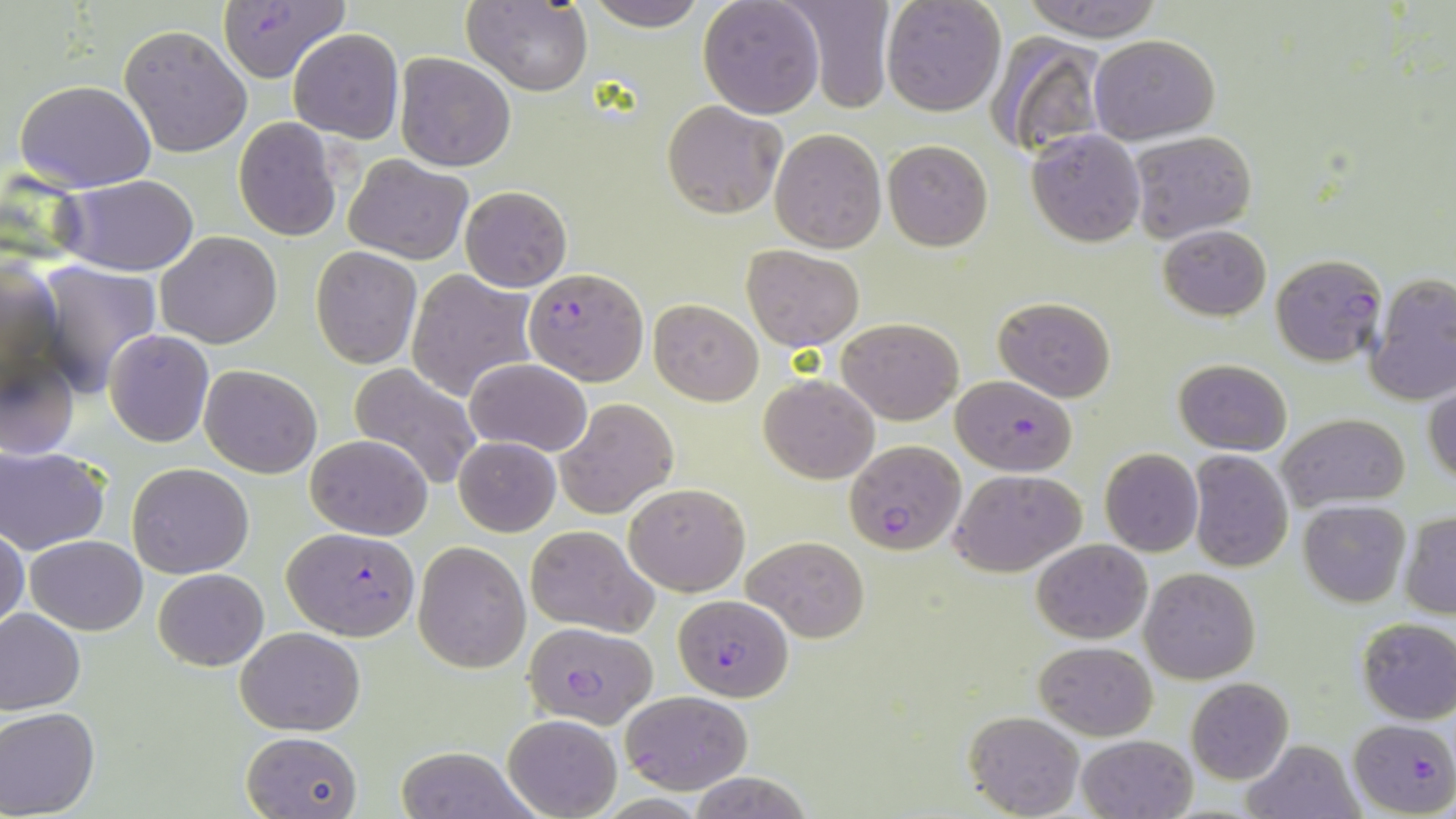
Approximate bounding boxes as (x1,y1)-(x2,y2) corner pairs in pixels. Uninfected red blood cell locations: (588,0)-(709,30), (696,0)-(825,119), (782,0)-(895,110), (880,0)-(1005,117), (1020,0)-(1164,41), (463,1)-(593,95), (119,24)-(253,158), (288,28)-(403,143), (987,32)-(1109,160), (1088,34)-(1219,143), (394,52)-(518,172), (252,54)-(377,204), (14,79)-(157,191), (662,101)-(785,218), (232,117)-(342,243), (1027,127)-(1145,247), (771,128)-(887,252), (1129,128)-(1256,243), (883,140)-(994,251), (343,155)-(472,263), (58,175)-(199,274), (460,185)-(571,292), (1158,223)-(1271,321), (157,231)-(283,348), (743,245)-(865,350), (311,246)-(423,368), (1271,253)-(1388,367), (1,257)-(63,402), (37,261)-(164,395), (409,268)-(534,401), (1365,274)-(1456,405), (994,296)-(1117,402), (649,299)-(763,405), (838,317)-(963,424), (104,330)-(213,447), (0,348)-(79,460), (466,358)-(591,456), (1173,359)-(1292,454), (199,364)-(323,478), (350,365)-(481,490), (761,375)-(879,483), (1425,386)-(1456,487), (554,398)-(679,518), (1277,412)-(1410,511), (306,433)-(433,540), (452,437)-(561,537), (1,445)-(110,554), (1099,448)-(1202,557), (1188,450)-(1295,572), (127,463)-(254,579), (949,466)-(1085,577), (623,483)-(750,596), (1298,500)-(1410,607), (1400,513)-(1456,618), (524,524)-(658,636), (0,525)-(28,634), (26,535)-(147,634), (742,535)-(870,642), (1031,538)-(1152,641), (413,542)-(531,672), (1139,567)-(1260,684), (154,568)-(268,669), (0,608)-(85,715), (1356,617)-(1456,723), (234,627)-(365,734), (1035,641)-(1157,739), (1187,678)-(1294,785), (0,706)-(100,817), (963,709)-(1085,818), (502,714)-(621,818), (240,730)-(362,819), (1076,734)-(1197,819), (1241,739)-(1364,819), (394,746)-(531,819), (691,773)-(811,817). Plasmodium falciparum-infected red blood cell locations: (217,2)-(349,82), (523,267)-(649,384), (952,376)-(1078,475), (844,439)-(966,555), (282,527)-(421,640), (674,595)-(793,701), (524,621)-(659,727), (619,690)-(752,793), (1349,718)-(1455,817). Slide-level diagnosis: Plasmodium falciparum. 1000x magnification. Thin blood smear. May-Grünwald-Giemsa stain. Light microscopy. Image is 1456×819 pixels. Single field of view.